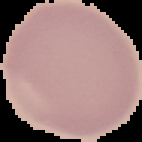

Summary:
  - Result: no Plasmodium parasites seen
  - Image type: segmented cell region with the area outside set to black
  - Image size: 142×142 pixels
  - Preparation: thin blood film